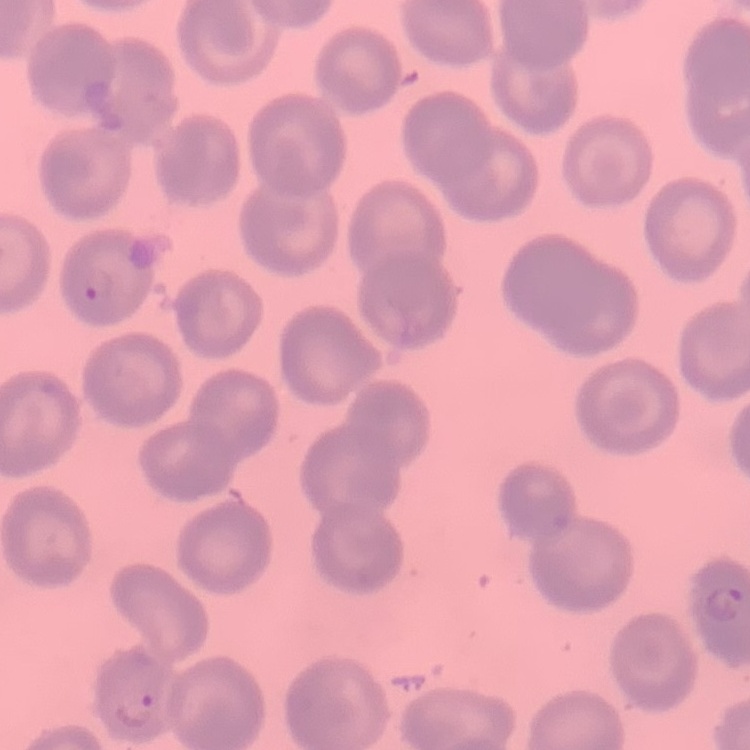
{
  "erythrocyte_morphology": "no rouleaux formation",
  "image_type": "one tile cut from a larger photomicrograph",
  "preparation": "thin peripheral smear",
  "stain": "Field's or Giemsa"
}